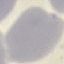

malaria status = uninfected
preparation = thin blood film
image type = automatically extracted cell patch, resized to 64 × 64 pixels
stain = Giemsa
capture = smartphone camera at the microscope eyepiece